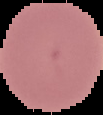
Image is 103×115 pixels. Malaria status: uninfected. From a thin blood film. Segmented cell region on a black background.